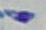

{
  "modality": "micrograph",
  "magnification": "1000x",
  "identification": "Toxoplasma gondii"
}